Assess the morphology of the erythrocytes.
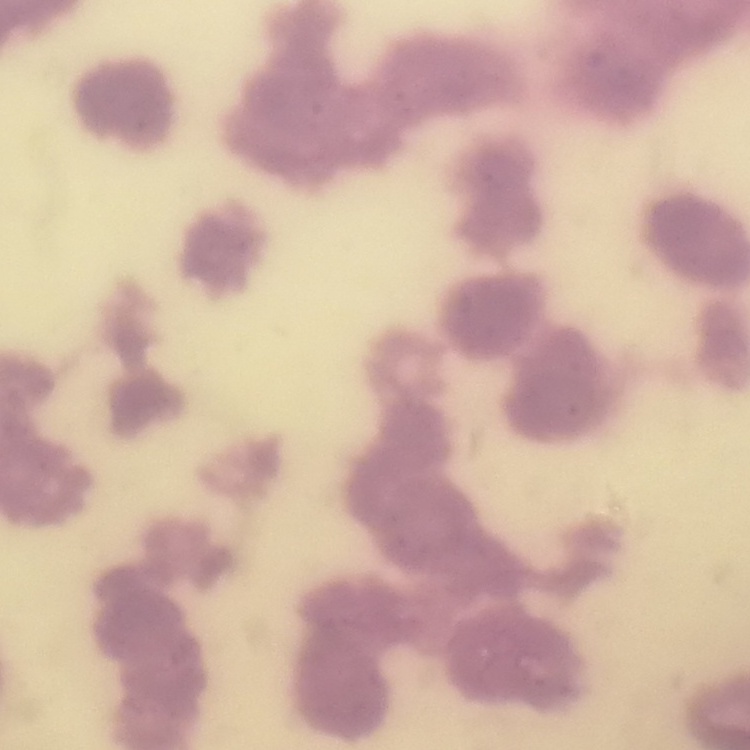
Rouleaux formation.

image type = one tile cut from a larger photomicrograph
stain = Field's or Giemsa
preparation = thin blood smear